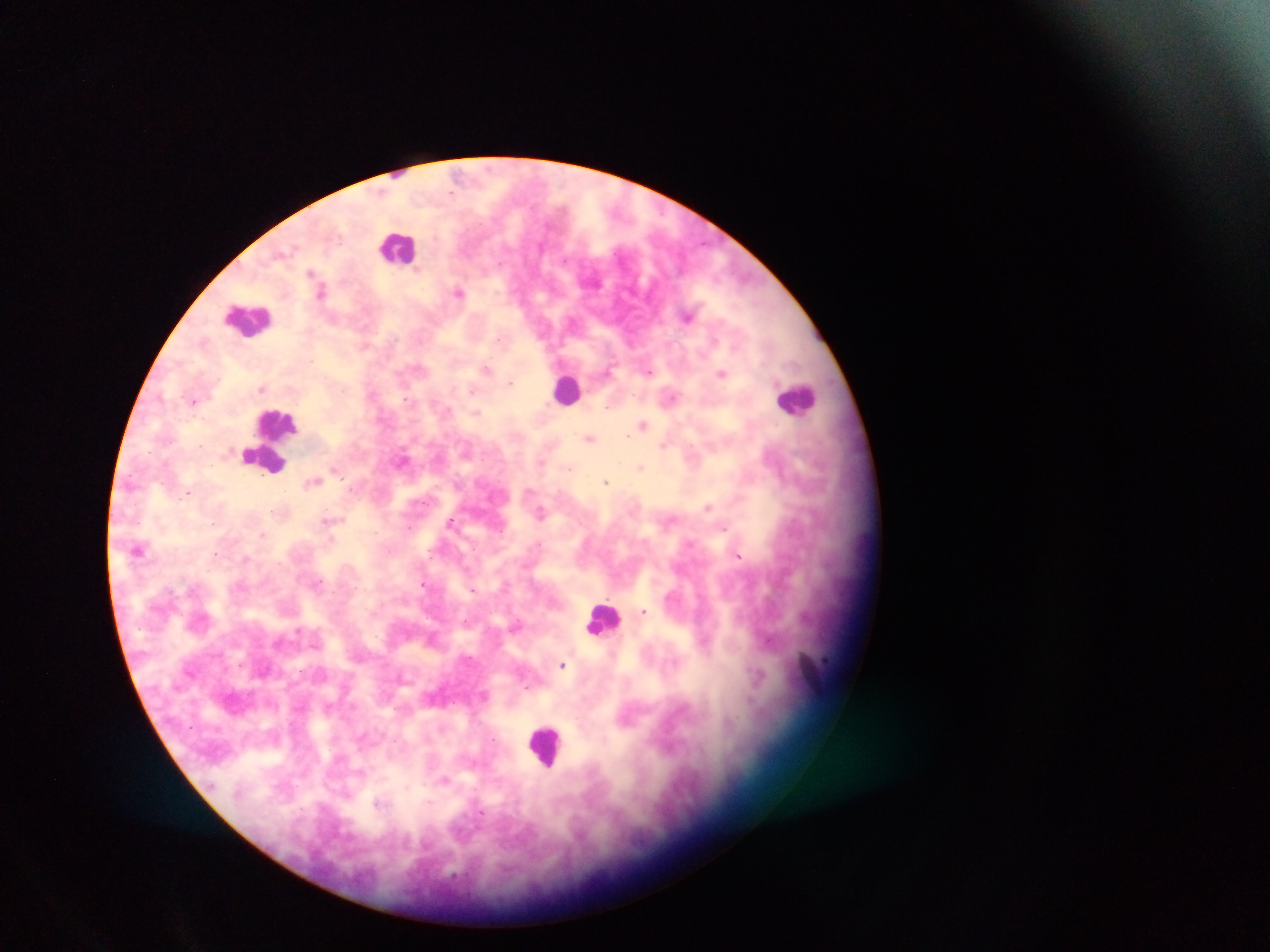

Approximate centers as x y in pixels.
Summary:
  - Malaria parasite locations: 310 271; 322 292; 460 292; 689 318; 736 346; 488 369; 648 372; 722 373; 511 382; 261 389; 473 389; 670 397; 194 403; 447 409; 478 411; 644 424; 639 428; 591 438; 663 446; 541 463; 641 466; 568 467; 336 468; 607 480; 314 482; 187 494; 708 506; 541 511; 333 518; 406 522; 452 522; 672 522; 726 528; 262 534; 139 550; 217 554; 739 556; 244 558; 239 582; 645 610; 563 665; 758 672; 446 778; 379 801
  - Leukocyte locations: 396 244; 248 321; 567 389; 795 400; 278 422; 263 459; 599 621; 816 677; 539 743
  - Image size: 1270×952 pixels
  - Field of view: single
  - Capture: mobile-phone photograph through a microscope
  - Preparation: thick blood smear
  - Country: Ghana